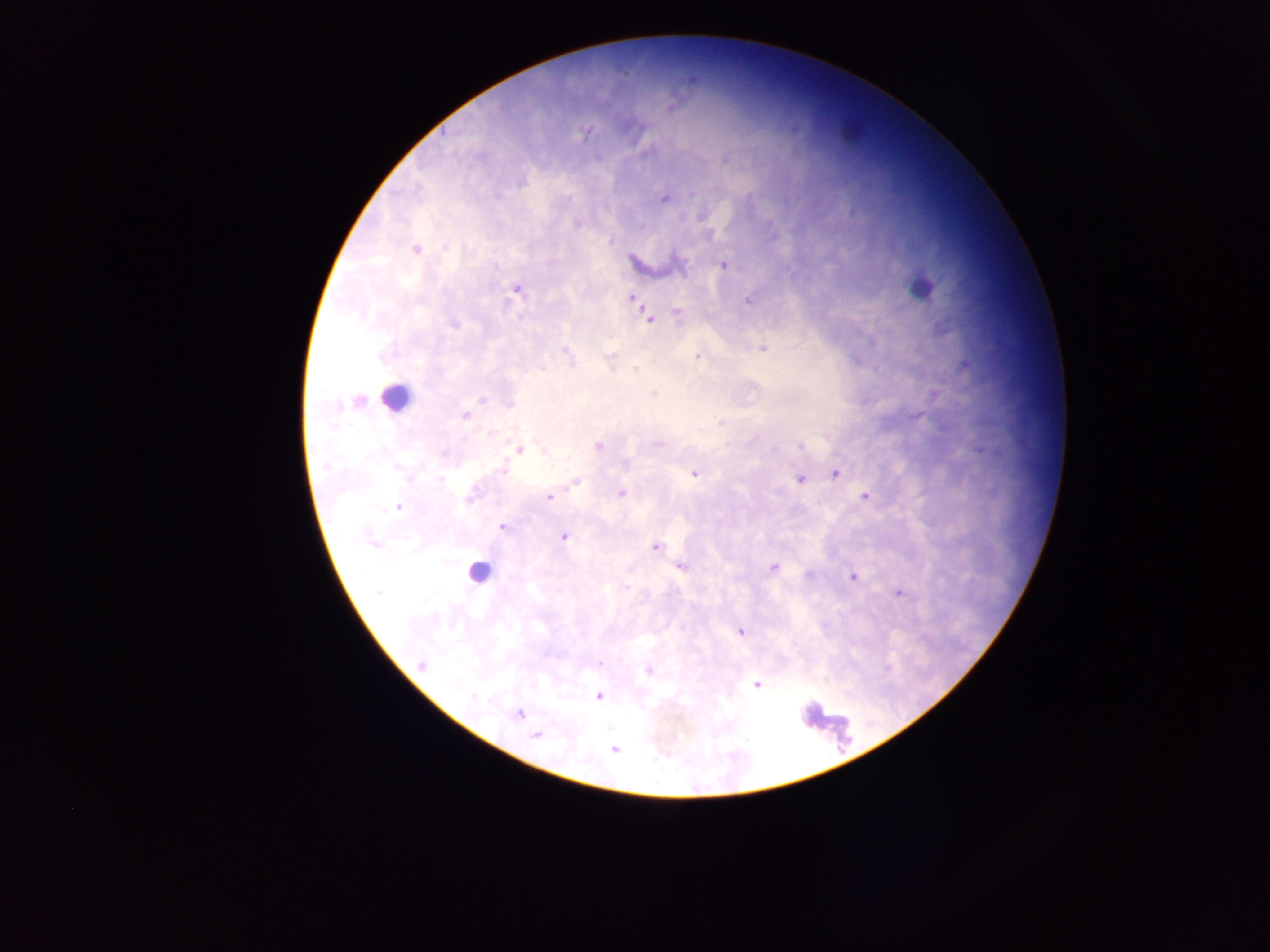

Approximate centers as {x, y} in pixels. Leukocyte locations: {921, 288}, {395, 397}, {477, 572}, {824, 725}. Malaria parasite locations: {586, 133}, {664, 198}, {415, 249}, {723, 264}, {515, 288}, {631, 296}, {748, 299}, {676, 312}, {648, 317}, {763, 346}, {565, 350}, {610, 356}, {697, 356}, {636, 369}, {654, 393}, {464, 416}, {598, 446}, {519, 448}, {502, 470}, {835, 472}, {694, 473}, {800, 478}, {575, 481}, {621, 494}, {865, 495}, {550, 496}, {398, 506}, {502, 526}, {563, 536}, {372, 540}, {654, 546}, {680, 565}, {773, 567}, {853, 575}, {898, 592}, {740, 631}, {421, 665}, {648, 671}, {756, 684}, {598, 695}, {518, 714}, {537, 735}, {614, 750}. One field of view. Thick blood smear. Image is 1270×952 pixels. Sample from Ghana. Photographed through a microscope with a mobile-phone camera.